Give the position of every Plasmodium falciparum parasite, noting its life-cycle stage.
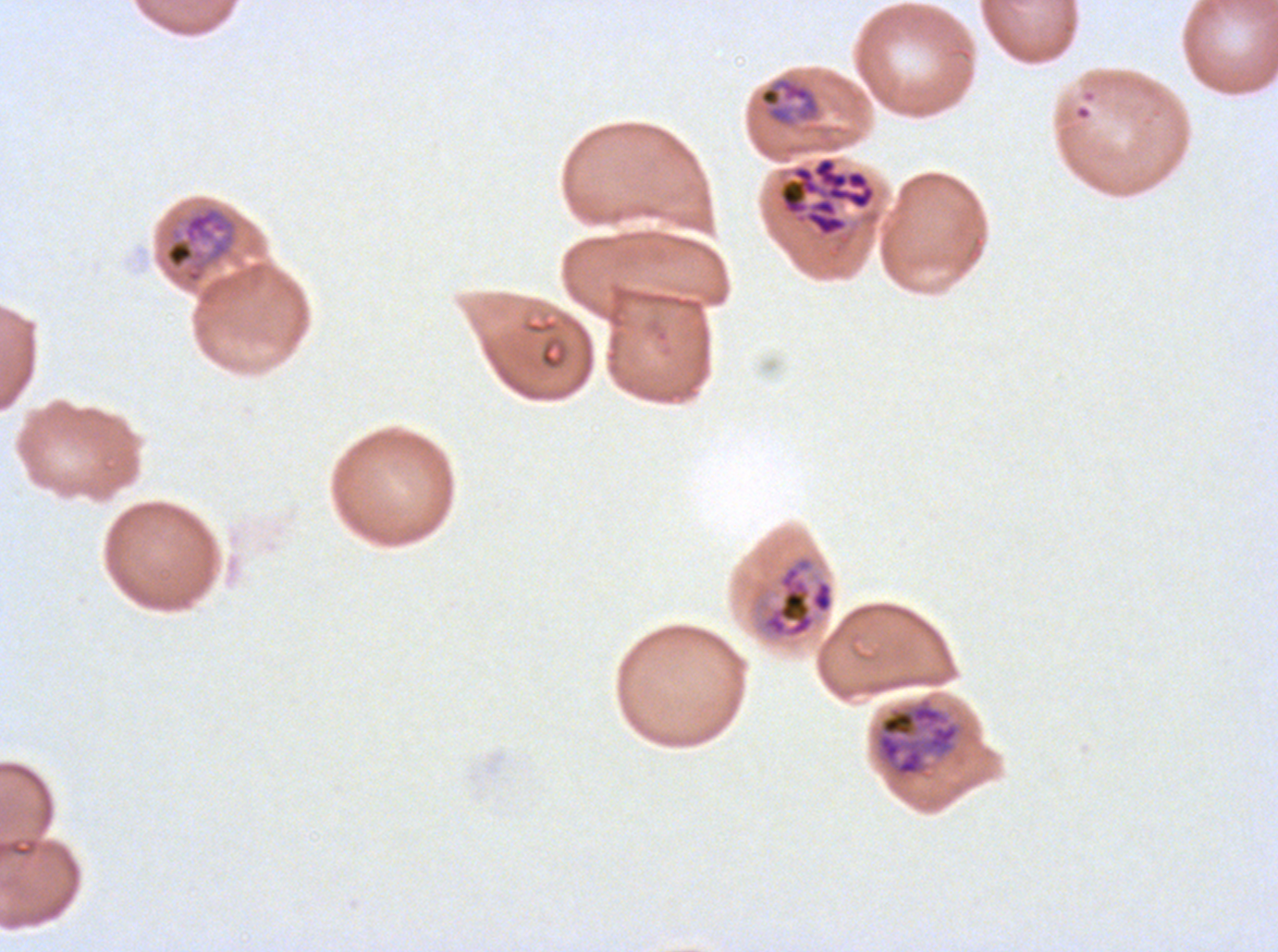
Approximate bounding boxes as [x1, y1, x2, y2] in pixels.
Mid trophozoites: [757, 76, 822, 128], [164, 204, 239, 284].
Late trophozoites: [749, 552, 835, 642], [875, 697, 960, 778].
Late schizonts: [779, 155, 877, 238].
No rings, late-ring/early-trophozoite forms, early schizonts, segmenters, or gametocytes observed.

field_of_view: one sub-image of a larger composite
stain: Giemsa
image_size: 1278×952 pixels
preparation: thin blood film
life_cycle_stages_observed: mid trophozoite, late trophozoite, late schizont
specimen: ex-vivo Plasmodium falciparum culture from a patient in The Gambia, grown for 24 to 48 hours